Identify the preparation type.
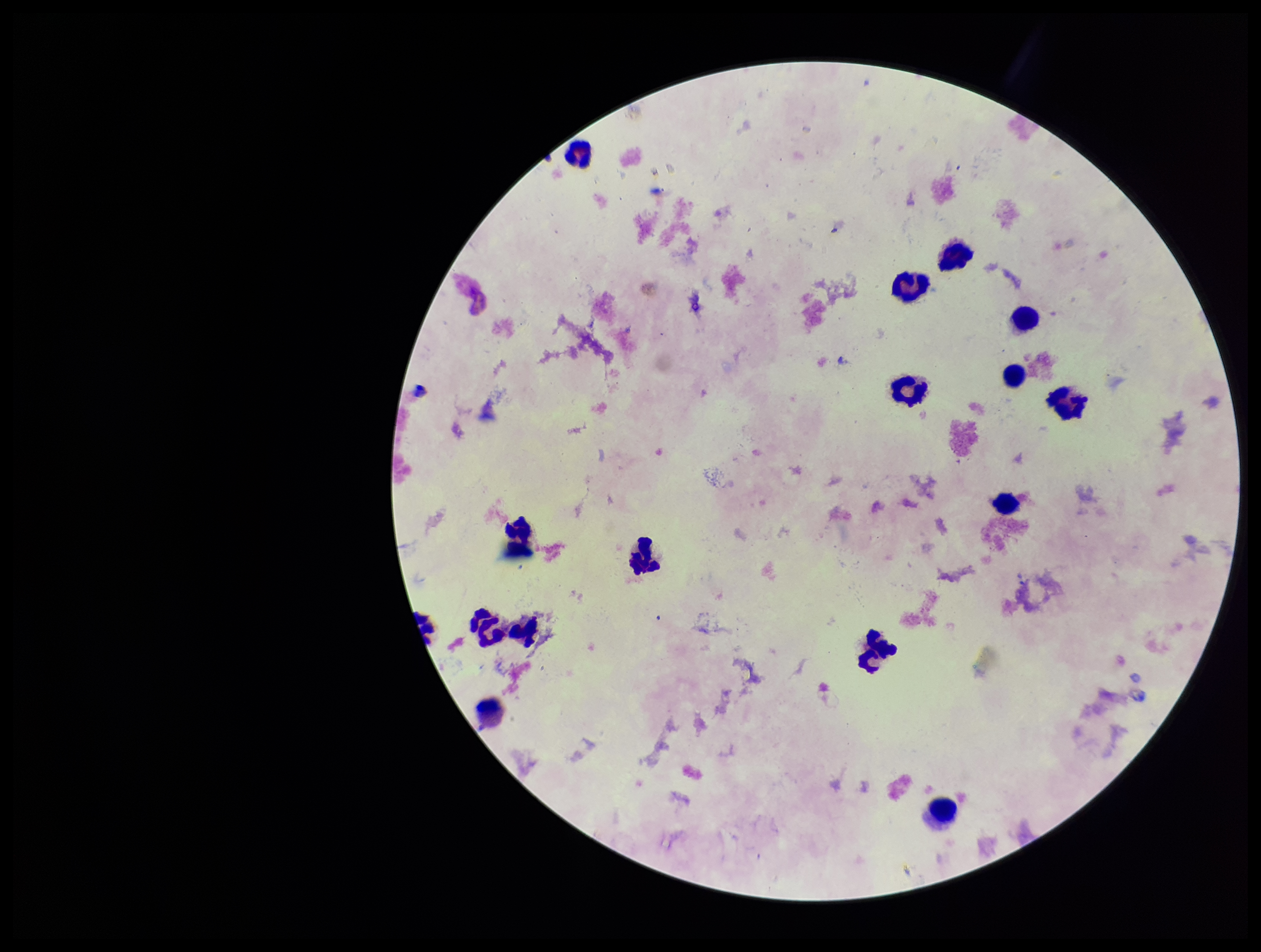

A thick smear.

image size = 1261×952 pixels
capture = smartphone photograph through the microscope eyepiece
patient malaria status = negative
leukocyte count = 15
parasite count = 0
stain = Giemsa
field of view = single
Plasmodium parasites = none seen